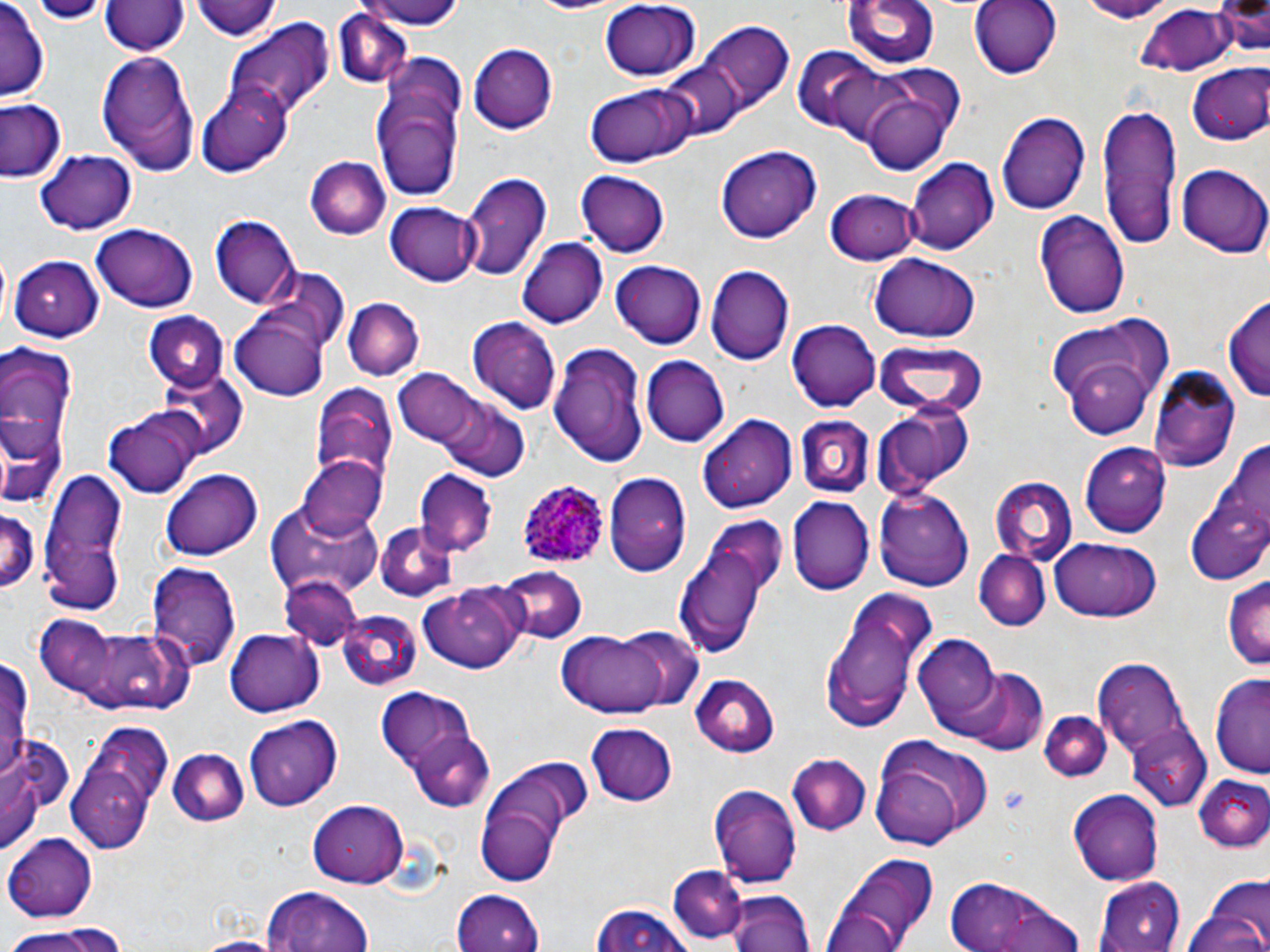

Summary:
  - Coordinate format: approximate bounding boxes as [x1, y1, x2, y2] in pixels
  - Uninfected red blood cell locations: [33, 0, 104, 23], [193, 0, 285, 41], [361, 0, 466, 30], [845, 0, 940, 71], [970, 0, 1063, 77], [1070, 0, 1174, 22], [101, 1, 188, 58], [1211, 1, 1269, 53], [597, 2, 700, 82], [0, 3, 48, 98], [1134, 7, 1231, 74], [332, 8, 413, 88], [224, 22, 333, 123], [694, 22, 793, 117], [468, 42, 559, 133], [791, 47, 910, 145], [97, 51, 201, 175], [370, 51, 469, 205], [663, 60, 744, 142], [1186, 64, 1270, 145], [585, 82, 693, 168], [197, 85, 293, 178], [864, 92, 952, 173], [0, 100, 67, 184], [1098, 105, 1182, 251], [997, 112, 1090, 216], [716, 145, 820, 244], [35, 150, 137, 236], [305, 156, 388, 241], [906, 156, 1000, 255], [1176, 163, 1270, 258], [577, 169, 671, 257], [461, 172, 553, 281], [831, 177, 997, 261], [825, 187, 920, 265], [387, 201, 480, 286], [1033, 207, 1132, 322], [213, 215, 300, 308], [92, 226, 198, 311], [517, 236, 607, 328], [10, 254, 105, 340], [868, 254, 980, 341], [609, 261, 707, 350], [706, 264, 795, 364], [260, 269, 347, 354], [1223, 293, 1270, 402], [342, 297, 424, 381], [143, 313, 227, 394], [231, 314, 329, 399], [1046, 314, 1175, 428], [466, 317, 561, 415], [788, 317, 880, 410], [872, 337, 986, 419], [548, 340, 650, 467], [0, 342, 78, 457], [641, 355, 729, 447], [1152, 366, 1241, 469], [392, 367, 483, 452], [157, 371, 246, 456], [310, 385, 397, 485], [438, 396, 529, 481], [871, 399, 975, 500], [0, 409, 65, 511], [104, 410, 201, 500], [698, 415, 798, 513], [794, 415, 874, 499], [1222, 435, 1269, 540], [1080, 444, 1168, 537], [295, 453, 389, 539], [40, 469, 127, 613], [414, 469, 496, 554], [161, 470, 262, 560], [604, 470, 691, 574], [991, 478, 1077, 566], [873, 487, 973, 591], [1187, 493, 1270, 587], [788, 497, 874, 595], [268, 501, 384, 596], [0, 505, 40, 594], [375, 524, 458, 600], [678, 535, 776, 660], [1049, 537, 1162, 624], [976, 550, 1050, 631], [147, 561, 242, 668], [492, 566, 587, 643], [280, 575, 364, 652], [1224, 579, 1270, 669], [418, 584, 528, 674], [821, 592, 942, 731], [338, 612, 421, 691], [38, 614, 196, 715], [614, 626, 704, 713], [227, 627, 323, 715], [559, 630, 673, 718], [911, 631, 1005, 732], [1092, 655, 1198, 776], [0, 659, 32, 780], [945, 668, 1048, 753], [1211, 672, 1270, 775], [690, 674, 782, 755], [372, 686, 477, 781], [1039, 710, 1111, 781], [245, 714, 343, 810], [586, 723, 679, 808], [1127, 727, 1211, 813], [66, 728, 167, 853], [406, 729, 496, 811], [5, 732, 75, 831], [868, 738, 990, 850], [171, 749, 249, 828], [2, 750, 45, 858], [787, 754, 871, 835], [475, 760, 583, 881], [1197, 774, 1269, 853], [709, 782, 801, 891], [1067, 789, 1165, 886], [308, 799, 406, 887], [5, 831, 98, 920], [826, 855, 939, 951], [668, 867, 747, 945], [940, 874, 1086, 952], [1094, 876, 1184, 952], [1186, 876, 1270, 952], [258, 886, 378, 952], [454, 889, 545, 952], [726, 889, 815, 952], [819, 901, 911, 951], [589, 903, 695, 952], [2, 923, 129, 952], [188, 935, 284, 952]
  - Plasmodium ovale-infected red blood cell locations: [518, 479, 607, 570]
  - Slide-level diagnosis: Plasmodium ovale
  - Image size: 1270×952 pixels
  - Magnification: 1000x
  - Stain: May-Grünwald-Giemsa
  - Field of view: one of a larger specimen
  - Modality: optical microscopy
  - Preparation: thin blood film